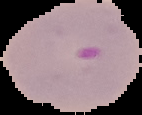
image size = 142×115 pixels
malaria status = parasitized
preparation = thin blood smear
image type = segmented cell region on a black background